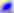
magnification = 400x
modality = micrograph
identification = Toxoplasma gondii